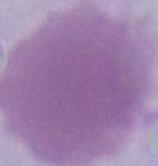
modality = micrograph
identification = red blood cell
magnification = 1000x